Assess this cell for malaria.
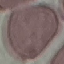
Uninfected.

Thin blood film. Photographed with a smartphone camera at the microscope eyepiece. Cell patch, automatically extracted from a larger field of view and resized to 64 × 64 pixels. Giemsa-stained preparation.